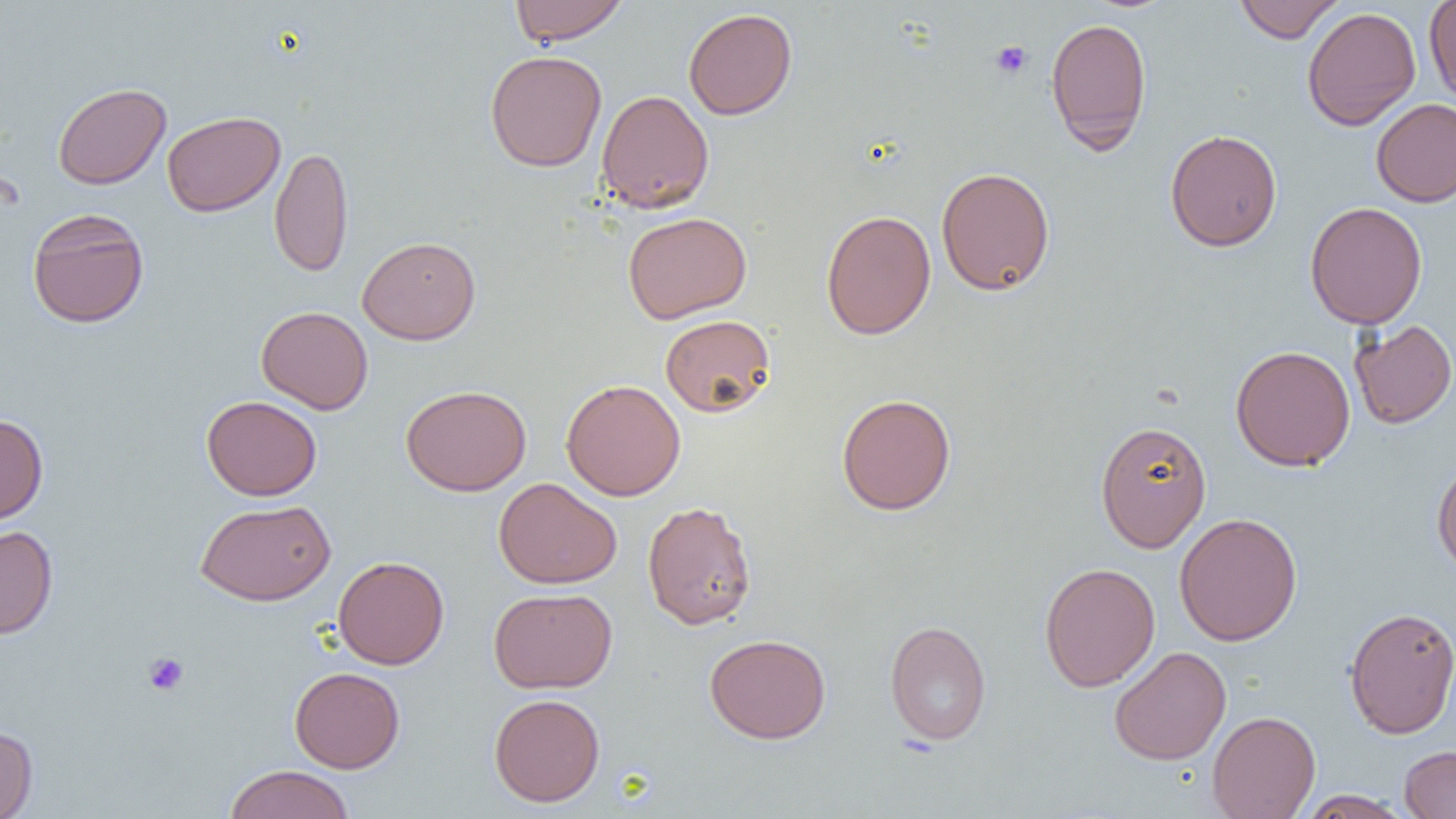

{
  "slide_level_diagnosis": "negative for blood parasites",
  "modality": "light microscopy",
  "platelet_locations": "approximate bounding boxes as [x1, y1, x2, y2] in pixels: [990, 40, 1032, 79], [143, 652, 189, 696]",
  "magnification": "1000x",
  "preparation": "thin blood smear",
  "field_of_view": "single",
  "uninfected_red_blood_cell_locations": "approximate bounding boxes as [x1, y1, x2, y2] in pixels: [510, 0, 629, 46], [1233, 0, 1345, 43], [1424, 0, 1456, 105], [1302, 6, 1421, 131], [683, 8, 797, 120], [1045, 16, 1152, 153], [485, 50, 607, 172], [53, 82, 171, 189], [597, 89, 714, 213], [1371, 98, 1456, 207], [161, 111, 286, 217], [1165, 129, 1282, 252], [269, 145, 354, 277], [935, 166, 1055, 296], [1304, 201, 1428, 329], [27, 208, 150, 328], [821, 209, 936, 340], [623, 212, 752, 324], [357, 235, 481, 345], [256, 306, 373, 415], [660, 314, 776, 417], [1349, 319, 1456, 429], [1230, 344, 1356, 472], [561, 379, 686, 501], [401, 384, 532, 496], [837, 393, 956, 515], [201, 395, 322, 500], [0, 414, 48, 524], [1095, 421, 1212, 552], [1431, 459, 1456, 578], [494, 477, 622, 589], [195, 499, 336, 605], [642, 501, 757, 630], [1174, 512, 1302, 646], [0, 526, 58, 638], [333, 555, 449, 669], [1039, 562, 1160, 692], [489, 587, 617, 693], [1343, 606, 1456, 738], [884, 620, 992, 745], [704, 633, 831, 744], [1109, 646, 1231, 765], [289, 666, 405, 772], [489, 693, 605, 807], [1207, 710, 1321, 819], [0, 725, 38, 819], [1399, 745, 1456, 818], [223, 764, 355, 819], [1296, 789, 1412, 818]",
  "image_size": "1456×819 pixels"
}